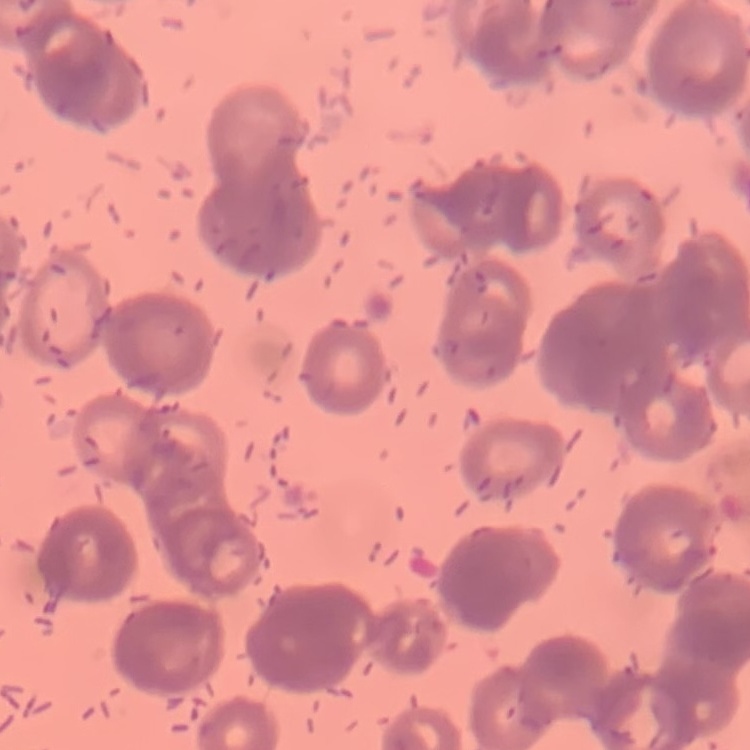

Summary:
  - Red blood cell morphology: rouleaux formation
  - Image type: square crop of a larger photomicrograph
  - Stain: Field's or Giemsa
  - Preparation: thin blood smear